Comment on the morphology of the red blood cells.
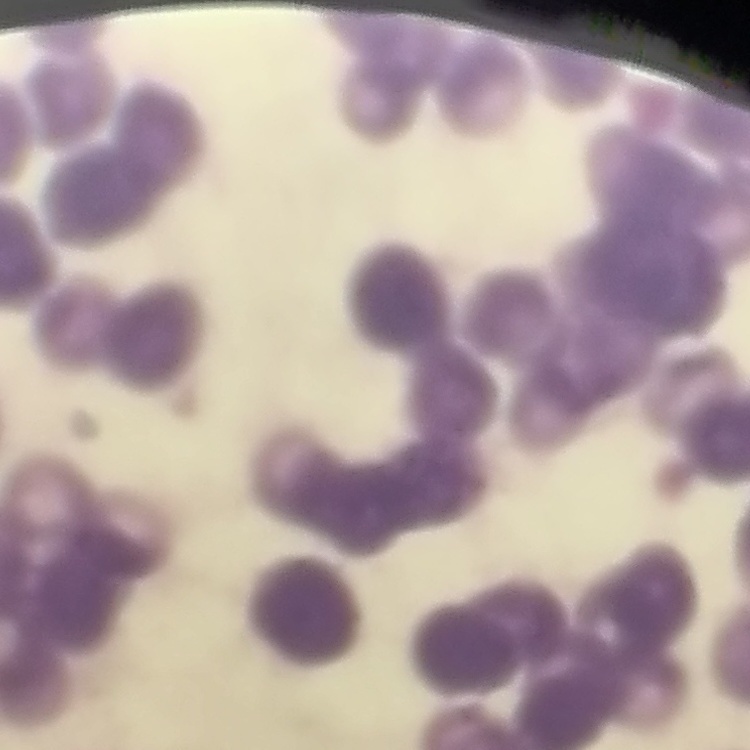

They show rouleaux formation.

One tile cut from a larger photomicrograph. Field's or Giemsa stain. Thin blood film.